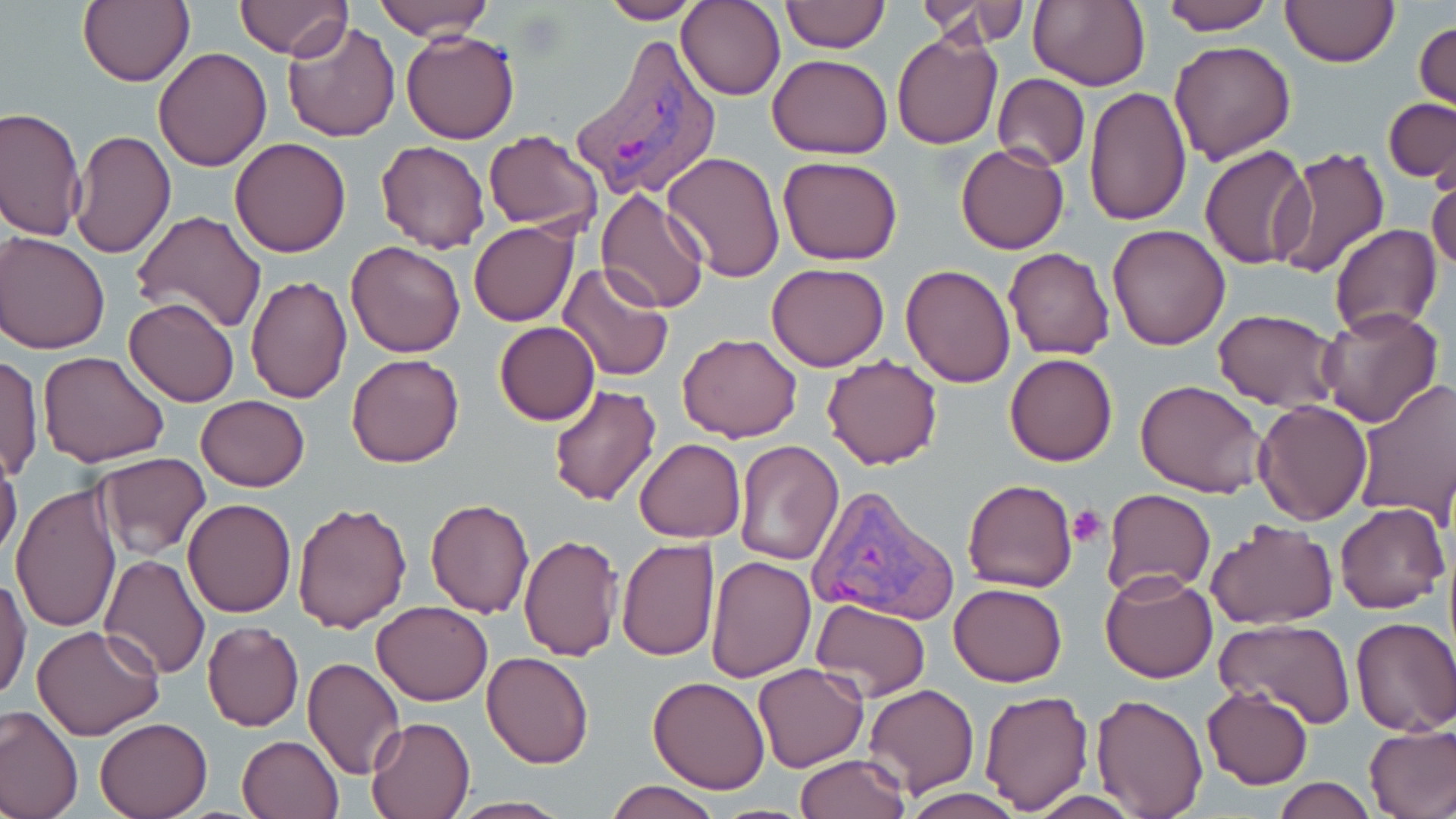

Approximate bounding boxes as named x1/y1/x2/y2 corners in pixels. Platelet locations: (x1=1066, y1=505, x2=1109, y2=547). Plasmodium vivax-infected red blood cell locations: (x1=572, y1=34, x2=721, y2=202), (x1=806, y1=483, x2=957, y2=625). Uninfected red blood cell locations: (x1=79, y1=0, x2=194, y2=87), (x1=373, y1=0, x2=492, y2=39), (x1=598, y1=0, x2=703, y2=24), (x1=679, y1=0, x2=785, y2=101), (x1=1027, y1=0, x2=1150, y2=92), (x1=1156, y1=0, x2=1271, y2=35), (x1=235, y1=1, x2=350, y2=59), (x1=782, y1=1, x2=887, y2=52), (x1=1280, y1=1, x2=1399, y2=68), (x1=921, y1=2, x2=1030, y2=47), (x1=241, y1=3, x2=376, y2=109), (x1=1414, y1=18, x2=1455, y2=115), (x1=281, y1=20, x2=400, y2=143), (x1=401, y1=29, x2=520, y2=145), (x1=893, y1=31, x2=1002, y2=150), (x1=1168, y1=41, x2=1296, y2=164), (x1=153, y1=47, x2=273, y2=171), (x1=768, y1=54, x2=893, y2=159), (x1=993, y1=73, x2=1089, y2=170), (x1=1084, y1=87, x2=1190, y2=227), (x1=1383, y1=98, x2=1456, y2=182), (x1=2, y1=107, x2=86, y2=242), (x1=482, y1=129, x2=602, y2=235), (x1=69, y1=130, x2=176, y2=258), (x1=229, y1=137, x2=352, y2=256), (x1=375, y1=141, x2=490, y2=254), (x1=955, y1=142, x2=1070, y2=254), (x1=1199, y1=143, x2=1315, y2=271), (x1=1271, y1=146, x2=1390, y2=281), (x1=661, y1=152, x2=784, y2=284), (x1=778, y1=156, x2=902, y2=266), (x1=1427, y1=165, x2=1456, y2=277), (x1=595, y1=188, x2=710, y2=314), (x1=129, y1=209, x2=267, y2=334), (x1=470, y1=221, x2=578, y2=326), (x1=1107, y1=223, x2=1232, y2=350), (x1=1329, y1=223, x2=1443, y2=339), (x1=1, y1=232, x2=110, y2=355), (x1=347, y1=240, x2=465, y2=357), (x1=1005, y1=247, x2=1115, y2=360), (x1=556, y1=262, x2=674, y2=382), (x1=766, y1=262, x2=890, y2=372), (x1=901, y1=264, x2=1016, y2=388), (x1=245, y1=276, x2=353, y2=403), (x1=124, y1=297, x2=239, y2=407), (x1=1315, y1=305, x2=1442, y2=429), (x1=1213, y1=308, x2=1344, y2=413), (x1=493, y1=321, x2=600, y2=424), (x1=676, y1=333, x2=803, y2=442), (x1=38, y1=351, x2=169, y2=467), (x1=1, y1=352, x2=43, y2=486), (x1=1005, y1=352, x2=1117, y2=466), (x1=821, y1=353, x2=944, y2=471), (x1=347, y1=354, x2=464, y2=468), (x1=1351, y1=378, x2=1456, y2=524), (x1=1136, y1=379, x2=1267, y2=500), (x1=547, y1=382, x2=662, y2=507), (x1=196, y1=394, x2=309, y2=492), (x1=1253, y1=399, x2=1373, y2=525), (x1=634, y1=438, x2=745, y2=542), (x1=733, y1=441, x2=845, y2=566), (x1=0, y1=453, x2=22, y2=566), (x1=96, y1=453, x2=211, y2=559), (x1=963, y1=478, x2=1077, y2=593), (x1=10, y1=484, x2=124, y2=636), (x1=1103, y1=488, x2=1214, y2=596), (x1=184, y1=499, x2=296, y2=618), (x1=425, y1=499, x2=535, y2=619), (x1=292, y1=500, x2=412, y2=633), (x1=1335, y1=501, x2=1449, y2=614), (x1=1205, y1=521, x2=1337, y2=630), (x1=518, y1=534, x2=624, y2=661), (x1=616, y1=537, x2=719, y2=661), (x1=99, y1=554, x2=210, y2=680), (x1=704, y1=555, x2=815, y2=683), (x1=1099, y1=570, x2=1218, y2=683), (x1=1, y1=575, x2=31, y2=705), (x1=948, y1=581, x2=1068, y2=687), (x1=811, y1=599, x2=931, y2=701), (x1=370, y1=600, x2=492, y2=705), (x1=1350, y1=616, x2=1456, y2=737), (x1=1214, y1=618, x2=1355, y2=728), (x1=32, y1=624, x2=165, y2=740), (x1=201, y1=624, x2=304, y2=731), (x1=481, y1=650, x2=595, y2=769), (x1=301, y1=657, x2=405, y2=779), (x1=752, y1=662, x2=868, y2=772), (x1=647, y1=675, x2=773, y2=794), (x1=863, y1=684, x2=980, y2=796), (x1=1201, y1=685, x2=1314, y2=789), (x1=977, y1=689, x2=1095, y2=812), (x1=1090, y1=693, x2=1209, y2=818), (x1=0, y1=705, x2=82, y2=819), (x1=94, y1=716, x2=214, y2=819), (x1=365, y1=716, x2=476, y2=819), (x1=1364, y1=722, x2=1456, y2=819), (x1=238, y1=735, x2=343, y2=819), (x1=794, y1=754, x2=911, y2=819), (x1=1271, y1=777, x2=1376, y2=818), (x1=605, y1=780, x2=723, y2=819), (x1=899, y1=788, x2=1024, y2=819), (x1=449, y1=797, x2=573, y2=818). Slide-level diagnosis: Plasmodium vivax. Thin blood film. Single field of view. Image is 1456×819 pixels. May-Grünwald-Giemsa-stained preparation. Light microscopy. 1000x magnification.